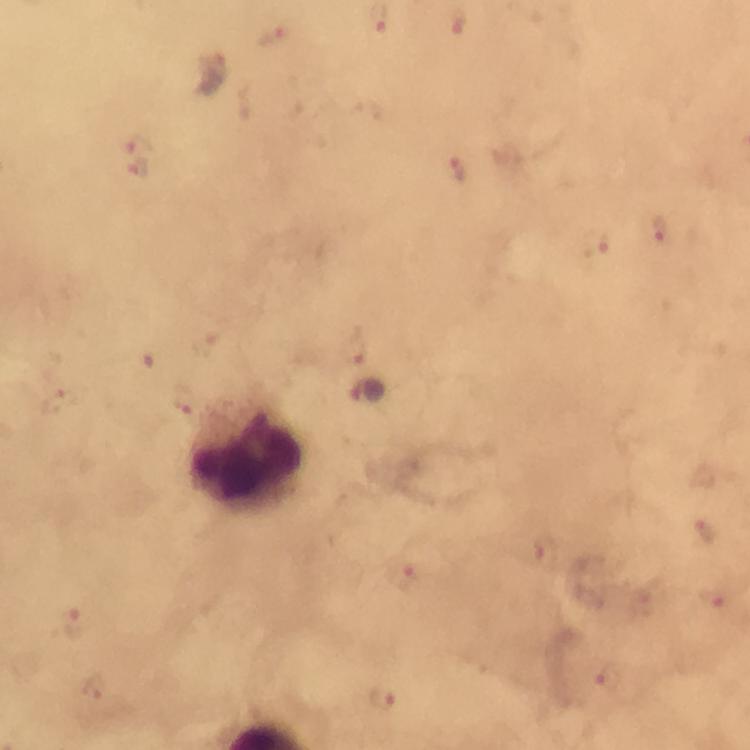
Approximate centers as [x, y] in pixels. Leukocyte locations: [247, 455]. Malaria parasite locations: [458, 22], [273, 37], [211, 74], [140, 143], [137, 168], [457, 170], [660, 229], [597, 245], [355, 346], [58, 399], [183, 400], [704, 530], [546, 550], [409, 578], [709, 604], [73, 622], [608, 677], [93, 688], [383, 696]. Image is 750×750 pixels. Immersion oil was used. From a diagnostic examination for malaria. A crop from one field of view. 100x magnification. Giemsa stain. Photographed with a smartphone mounted on the microscope. Thick blood film.